Name the parasite shown.
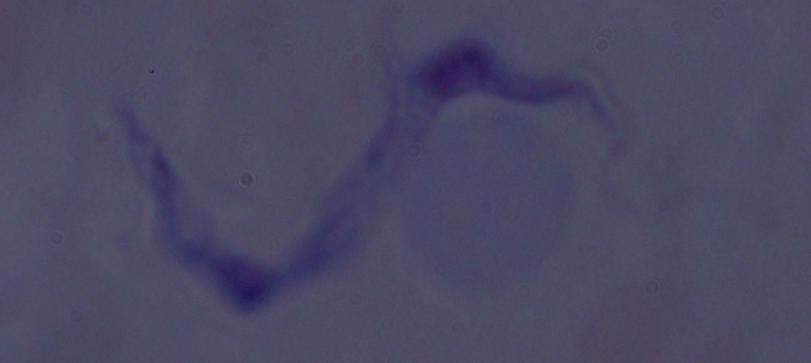

A trypanosome.

Photomicrograph. Captured at 1000x magnification.